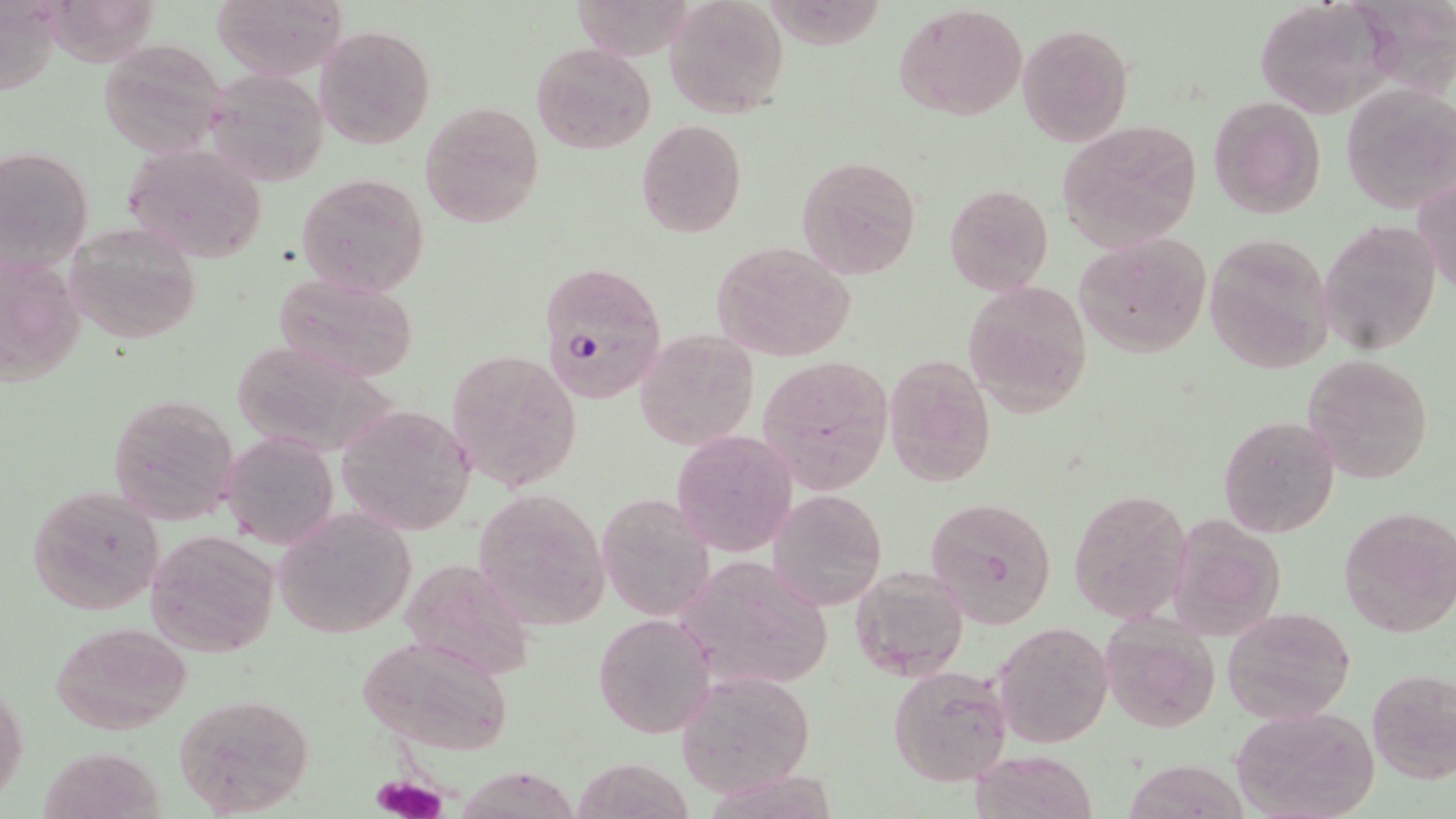

Summary:
  - Coordinate format: approximate bounding boxes as [x1, y1, x2, y2] in pixels
  - Uninfected red blood cell locations: [210, 0, 346, 79], [663, 0, 790, 118], [1252, 0, 1394, 118], [895, 3, 1027, 121], [1017, 23, 1133, 145], [315, 25, 435, 148], [96, 38, 231, 158], [531, 42, 655, 153], [202, 71, 331, 186], [1341, 81, 1454, 214], [1207, 96, 1326, 219], [419, 101, 545, 228], [635, 118, 747, 238], [1057, 119, 1204, 248], [120, 141, 268, 264], [0, 143, 95, 276], [797, 155, 922, 280], [296, 172, 430, 298], [1414, 176, 1456, 292], [943, 183, 1053, 295], [1318, 218, 1441, 358], [64, 223, 202, 344], [1073, 233, 1212, 356], [1202, 234, 1335, 374], [710, 240, 856, 361], [0, 265, 92, 399], [273, 274, 420, 383], [962, 280, 1094, 416], [635, 328, 759, 449], [448, 348, 583, 490], [1302, 353, 1434, 484], [757, 354, 892, 493], [882, 355, 995, 487], [104, 394, 238, 525], [341, 409, 478, 531], [1218, 415, 1340, 539], [672, 430, 797, 556], [224, 433, 338, 548], [25, 484, 165, 617], [470, 488, 609, 630], [768, 490, 887, 609], [1068, 490, 1193, 623], [597, 494, 716, 622], [924, 496, 1060, 629], [1341, 506, 1456, 638], [271, 509, 417, 640], [1165, 515, 1285, 639], [144, 528, 281, 659], [673, 553, 835, 690], [398, 555, 536, 680], [849, 563, 970, 682], [1222, 607, 1356, 723], [593, 611, 715, 739], [1097, 615, 1220, 733], [50, 621, 192, 734], [991, 621, 1115, 748], [352, 633, 516, 756], [887, 663, 1015, 786], [1367, 667, 1456, 785], [676, 670, 818, 797], [0, 683, 28, 806], [170, 692, 316, 816], [1229, 706, 1379, 819], [40, 744, 166, 819], [970, 750, 1098, 819], [570, 758, 697, 818], [453, 763, 595, 819]
  - Platelet locations: [370, 774, 447, 819]
  - Plasmodium falciparum-infected red blood cell locations: [537, 261, 667, 406]
  - Slide-level diagnosis: Plasmodium falciparum
  - Preparation: thin blood film
  - Field of view: one of a larger specimen
  - Magnification: 1000x
  - Modality: optical microscopy
  - Image size: 1456×819 pixels
  - Stain: May-Grünwald-Giemsa